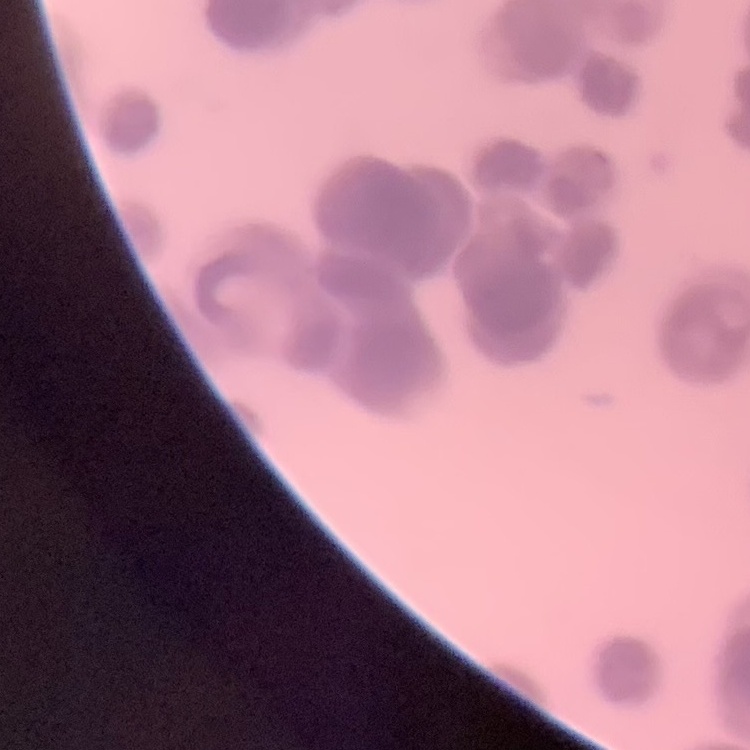

The erythrocytes exhibit rouleaux formation. Square crop of a larger photomicrograph. Thin blood smear. Stained with either Field's or Giemsa.